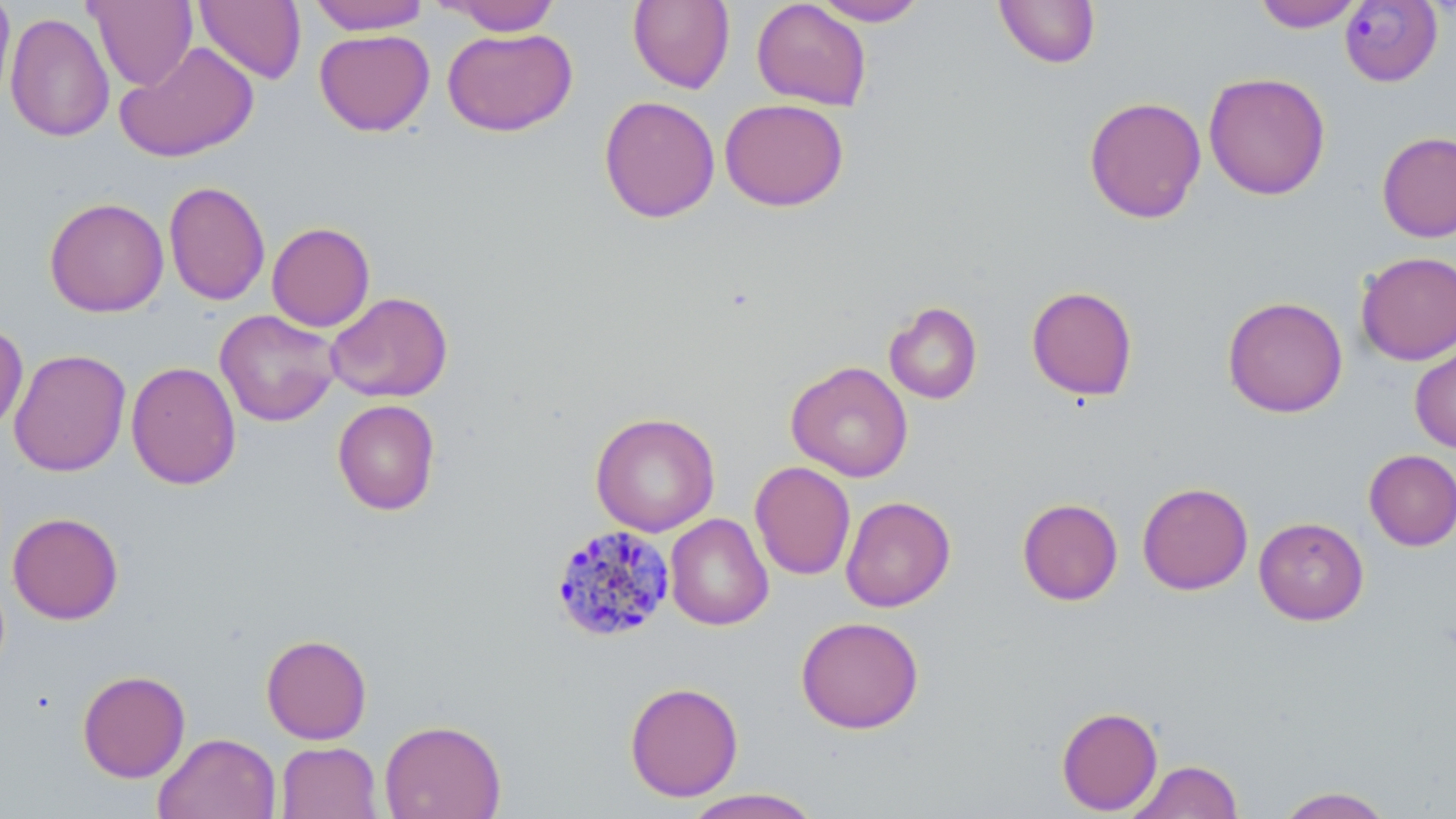
{
  "slide_level_diagnosis": "Plasmodium malariae",
  "modality": "light microscopy",
  "image_size": "1456×819 pixels",
  "field_of_view": "single",
  "uninfected_red_blood_cell_locations": "approximate bounding boxes as [x1, y1, x2, y2] in pixels: [0, 0, 16, 108], [84, 0, 198, 91], [194, 0, 306, 84], [308, 0, 429, 34], [751, 0, 872, 111], [810, 0, 929, 26], [994, 0, 1101, 68], [1252, 0, 1365, 32], [441, 1, 561, 36], [627, 1, 735, 93], [5, 12, 115, 143], [441, 28, 578, 136], [314, 29, 435, 136], [115, 40, 259, 162], [1203, 72, 1331, 200], [598, 95, 721, 223], [1083, 95, 1206, 224], [719, 97, 849, 211], [1376, 131, 1456, 243], [164, 181, 270, 306], [44, 197, 169, 317], [267, 222, 375, 332], [1355, 251, 1456, 365], [1026, 285, 1138, 401], [325, 291, 453, 403], [1222, 296, 1348, 418], [884, 301, 983, 405], [215, 309, 341, 427], [0, 320, 29, 434], [1409, 338, 1456, 453], [8, 349, 130, 477], [126, 361, 242, 490], [786, 361, 913, 482], [332, 398, 441, 516], [590, 411, 720, 537], [1364, 449, 1456, 551], [749, 461, 856, 580], [1137, 482, 1253, 595], [840, 495, 956, 612], [1017, 498, 1123, 605], [7, 512, 124, 625], [664, 513, 774, 631], [1254, 516, 1369, 625], [795, 616, 924, 734], [261, 634, 372, 744], [77, 669, 191, 783], [624, 681, 744, 802], [1056, 706, 1163, 815], [379, 718, 506, 819], [153, 732, 281, 819], [275, 741, 382, 819], [1127, 760, 1244, 818], [1273, 786, 1395, 818], [680, 788, 824, 818]",
  "plasmodium_malariae_infected_red_blood_cell_locations": "approximate bounding boxes as [x1, y1, x2, y2] in pixels: [1339, 1, 1443, 87], [549, 524, 676, 642]",
  "stain": "May-Grünwald-Giemsa",
  "magnification": "1000x",
  "preparation": "thin blood smear"
}